Identify the preparation type.
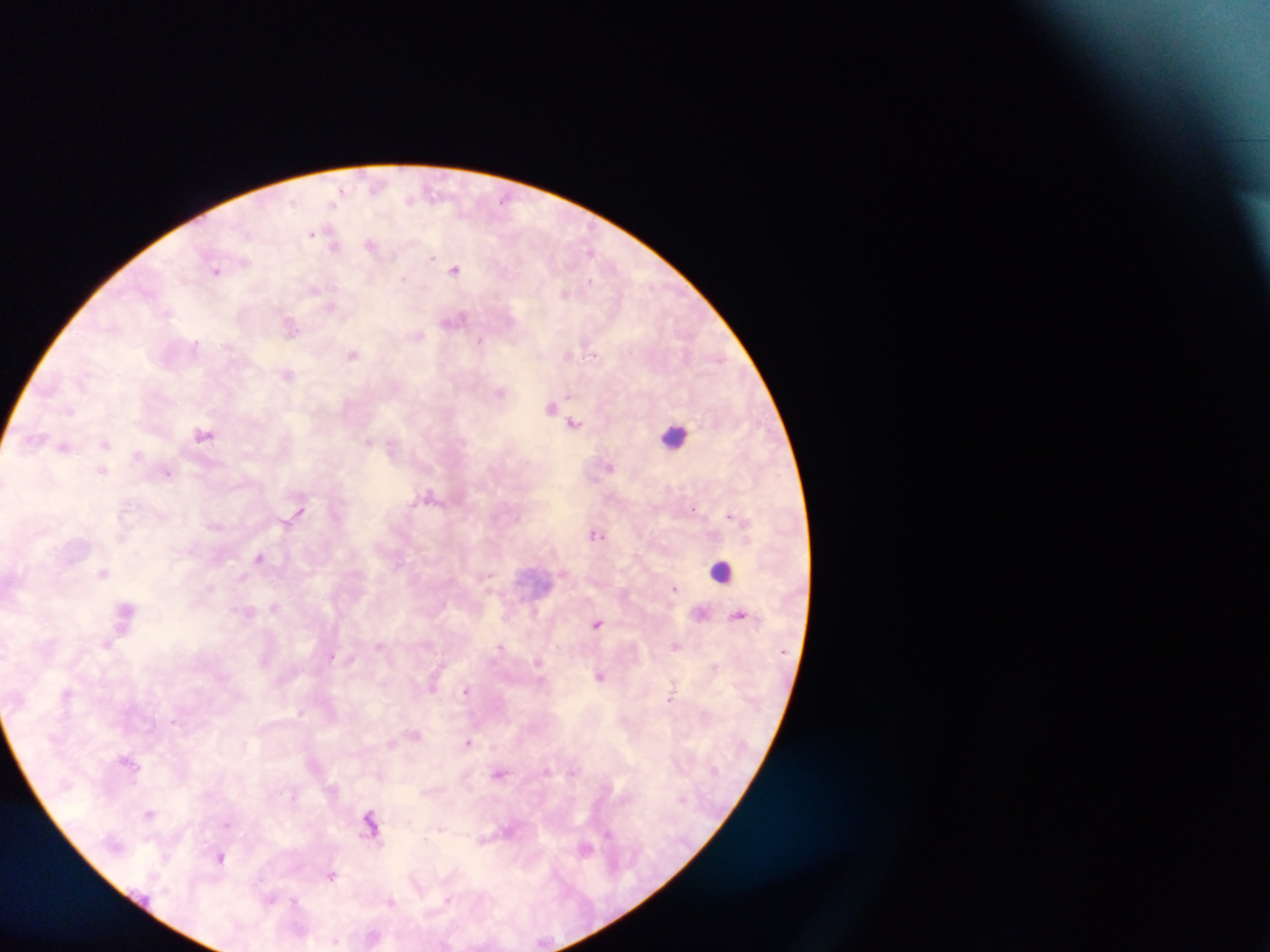
Thick blood film.

Approximate centers as (x, y) in pixels.
Summary:
  - Leukocyte locations: (674, 435), (722, 570)
  - Malaria parasite locations: (376, 186), (433, 192), (410, 199), (335, 200), (504, 200), (311, 232), (371, 245), (334, 246), (591, 252), (432, 257), (455, 269), (216, 270), (589, 282), (314, 289), (565, 293), (332, 306), (167, 313), (454, 320), (291, 325), (419, 335), (481, 340), (196, 344), (592, 352), (568, 353), (353, 355), (720, 359), (287, 374), (500, 392), (551, 407), (71, 410), (575, 423), (203, 434), (36, 440), (367, 441), (105, 444), (64, 446), (138, 455), (609, 467), (102, 471), (167, 473), (429, 496), (692, 508), (729, 516), (595, 534), (259, 557), (103, 573), (489, 576), (674, 588), (275, 607), (126, 608), (249, 612), (740, 614), (597, 623), (107, 644), (380, 646), (675, 646), (500, 647), (331, 656), (539, 663), (601, 676), (466, 690), (671, 695), (300, 712), (468, 742), (573, 773), (500, 774), (149, 814), (370, 824), (226, 825), (608, 833), (585, 848), (221, 858), (331, 876), (270, 900), (295, 900), (447, 900), (390, 902), (334, 941)
  - Capture: mobile-phone photograph through a microscope
  - Field of view: single
  - Country: Ghana
  - Image size: 1270×952 pixels